Identify the preparation type.
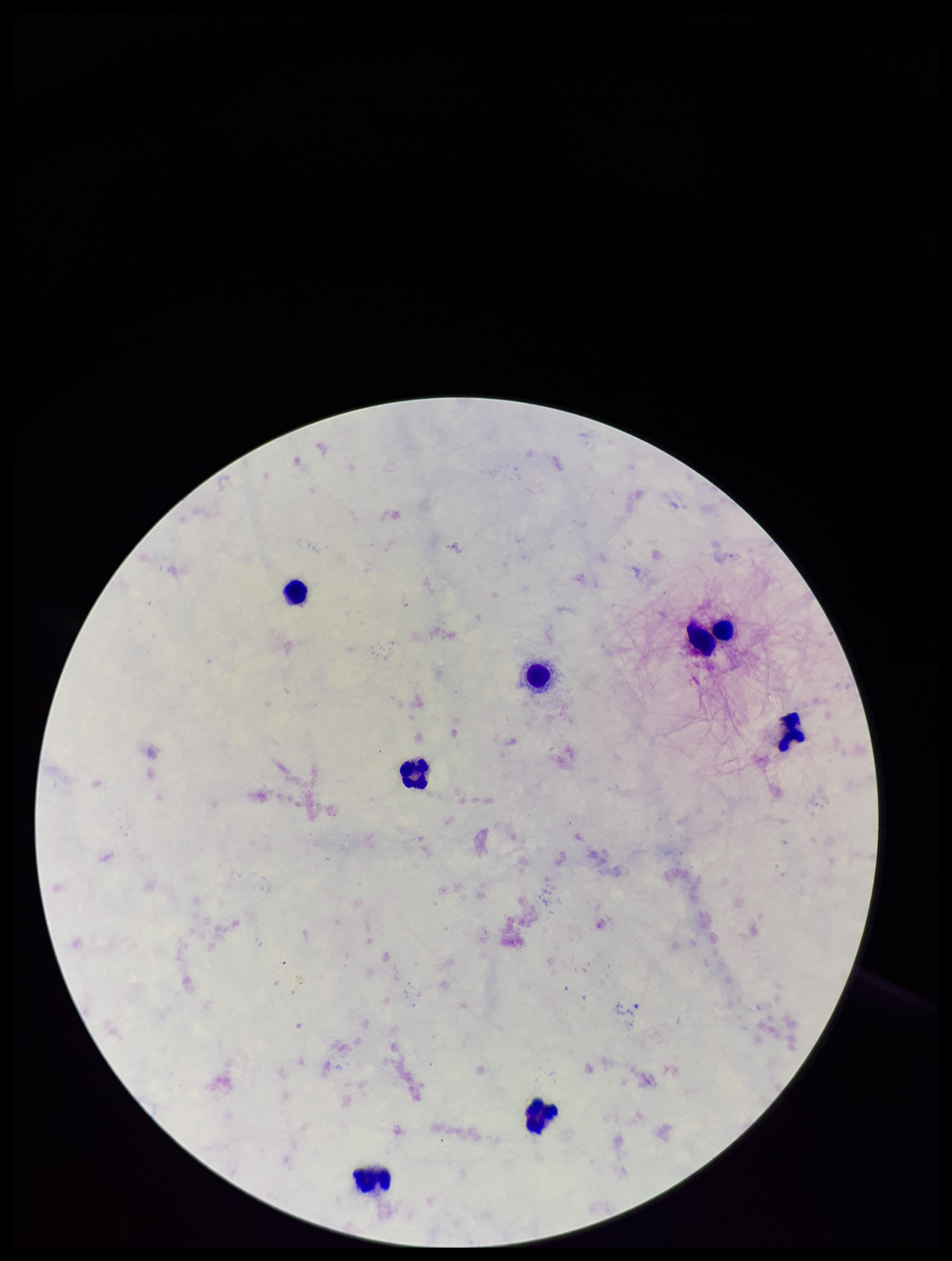
A thick smear.

capture = smartphone photograph through the microscope eyepiece
image size = 952×1261 pixels
field of view = one from this slide
parasite count = 0
species reported for this patient = Plasmodium falciparum
patient malaria status = infected
stain = Giemsa
Plasmodium parasites = none identified
leukocyte count = 8